Locate and identify every blood parasite.
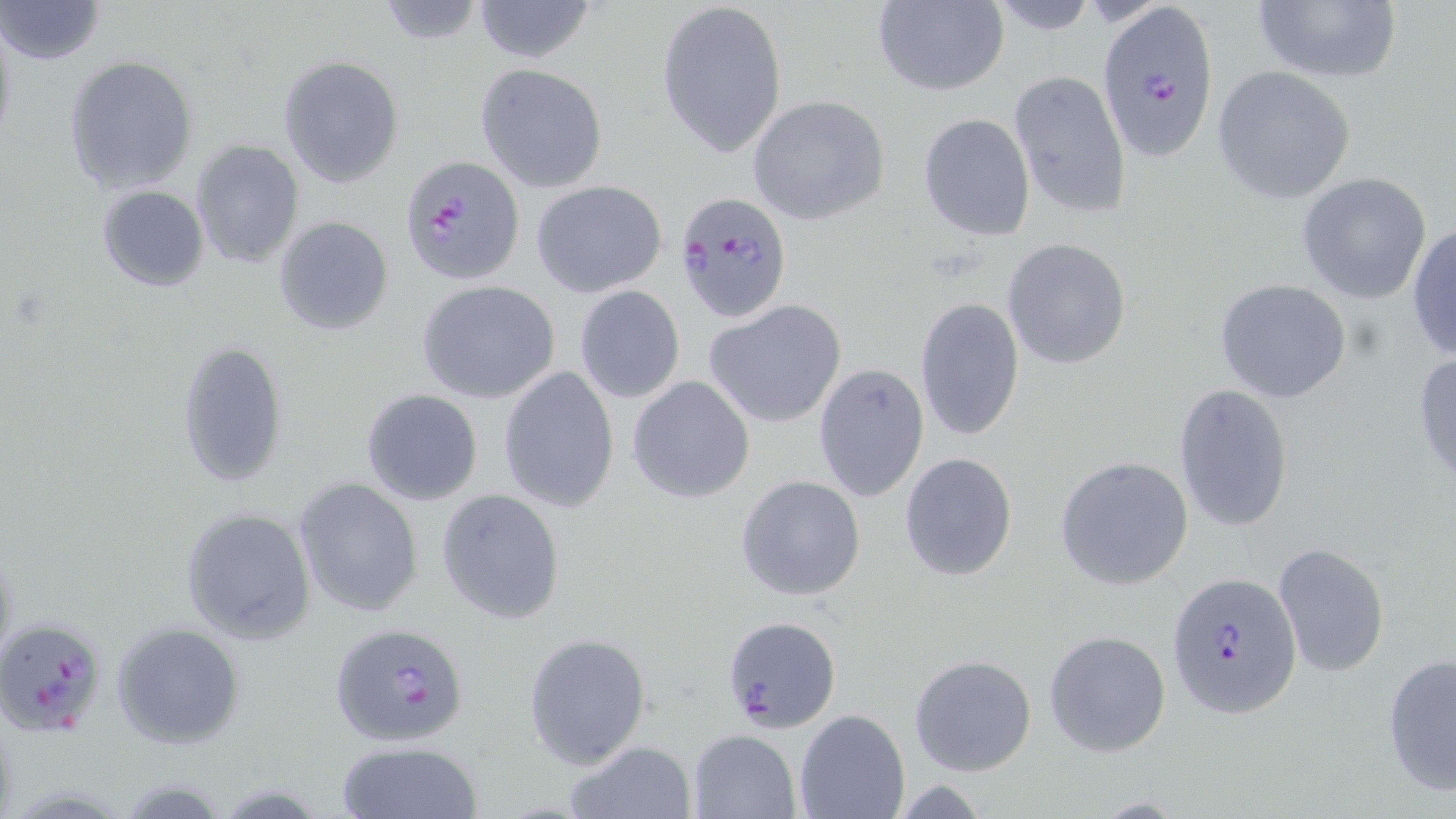
Approximate bounding boxes as named x1/y1/x2/y2 corners in pixels.
Plasmodium falciparum-infected red blood cells: (x1=1098, y1=2, x2=1221, y2=159), (x1=399, y1=154, x2=523, y2=286), (x1=675, y1=191, x2=793, y2=324), (x1=1167, y1=573, x2=1301, y2=718), (x1=3, y1=615, x2=108, y2=738), (x1=721, y1=615, x2=842, y2=732), (x1=331, y1=622, x2=468, y2=747).
No Plasmodium ovale, Plasmodium malariae, Plasmodium vivax, Babesia divergens, or Trypanosoma brucei observed.

Uninfected red blood cell locations: (x1=1, y1=0, x2=104, y2=66), (x1=471, y1=0, x2=597, y2=63), (x1=655, y1=0, x2=787, y2=158), (x1=873, y1=0, x2=1007, y2=97), (x1=1250, y1=0, x2=1401, y2=84), (x1=375, y1=1, x2=485, y2=45), (x1=0, y1=16, x2=17, y2=157), (x1=64, y1=54, x2=198, y2=196), (x1=279, y1=55, x2=404, y2=187), (x1=475, y1=64, x2=608, y2=193), (x1=1212, y1=65, x2=1356, y2=203), (x1=1008, y1=70, x2=1130, y2=222), (x1=747, y1=94, x2=890, y2=226), (x1=918, y1=112, x2=1035, y2=242), (x1=192, y1=140, x2=303, y2=268), (x1=1298, y1=172, x2=1432, y2=303), (x1=532, y1=180, x2=667, y2=299), (x1=97, y1=184, x2=209, y2=291), (x1=273, y1=216, x2=395, y2=335), (x1=1407, y1=222, x2=1456, y2=362), (x1=1002, y1=238, x2=1133, y2=370), (x1=1213, y1=279, x2=1354, y2=404), (x1=416, y1=280, x2=559, y2=404), (x1=573, y1=285, x2=685, y2=404), (x1=915, y1=296, x2=1025, y2=442), (x1=705, y1=300, x2=845, y2=428), (x1=176, y1=341, x2=288, y2=487), (x1=1412, y1=350, x2=1456, y2=487), (x1=812, y1=362, x2=929, y2=503), (x1=498, y1=365, x2=618, y2=512), (x1=627, y1=375, x2=755, y2=503), (x1=1173, y1=384, x2=1294, y2=531), (x1=361, y1=388, x2=483, y2=505), (x1=899, y1=453, x2=1018, y2=580), (x1=1054, y1=455, x2=1194, y2=592), (x1=735, y1=474, x2=866, y2=602), (x1=294, y1=477, x2=424, y2=616), (x1=435, y1=488, x2=566, y2=625), (x1=179, y1=508, x2=314, y2=644), (x1=1272, y1=542, x2=1390, y2=678), (x1=112, y1=624, x2=244, y2=748), (x1=1044, y1=630, x2=1171, y2=757), (x1=523, y1=632, x2=652, y2=768), (x1=909, y1=653, x2=1036, y2=775), (x1=1382, y1=653, x2=1456, y2=796), (x1=794, y1=709, x2=908, y2=819), (x1=688, y1=729, x2=800, y2=817), (x1=562, y1=740, x2=696, y2=819), (x1=335, y1=741, x2=482, y2=819). Slide-level diagnosis: Plasmodium falciparum. One field of a larger specimen. Captured at 1000x magnification. Light microscopy. May-Grünwald-Giemsa-stained preparation. Image is 1456×819 pixels. Thin blood smear.